Name the cell type shown.
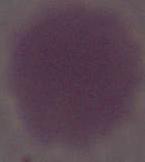

An erythrocyte.

magnification = 1000x
modality = photomicrograph